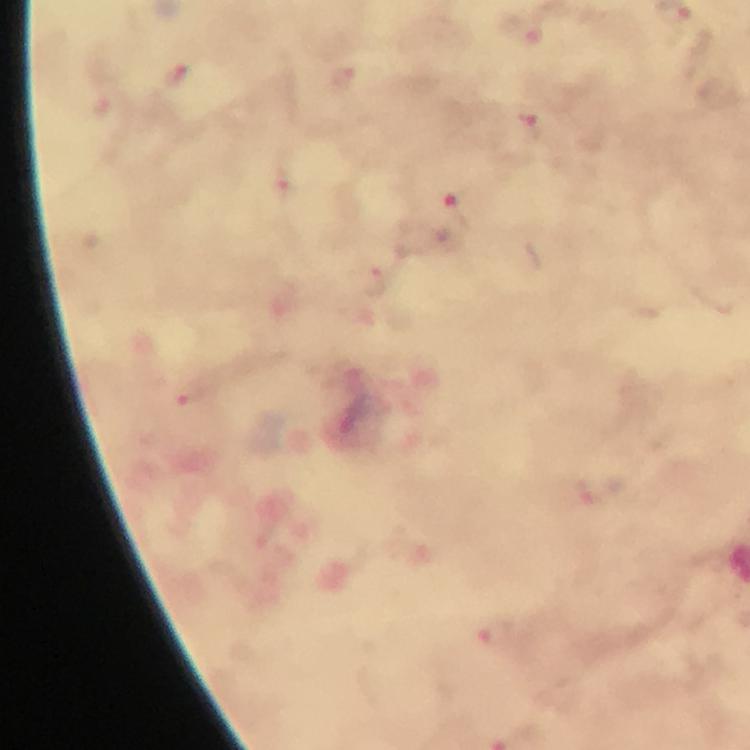
{
  "context": "from a malaria diagnostic workup",
  "capture": "smartphone mounted on the microscope",
  "cropped_from": "one field of view",
  "immersion_oil": "used",
  "preparation": "thick blood smear",
  "stain": "Giemsa",
  "plasmodium_parasite_locations": "approximate centers as {x, y} in pixels: {457, 210}, {189, 395}, {591, 491}, {500, 635}",
  "image_size": "750×750 pixels",
  "magnification": "100x"
}